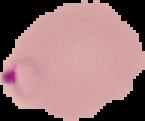
{
  "result": "Plasmodium parasites detected",
  "image_size": "145×121 pixels",
  "image_type": "cell region segmented out of the field of view; surrounding area masked to black",
  "preparation": "thin blood film"
}